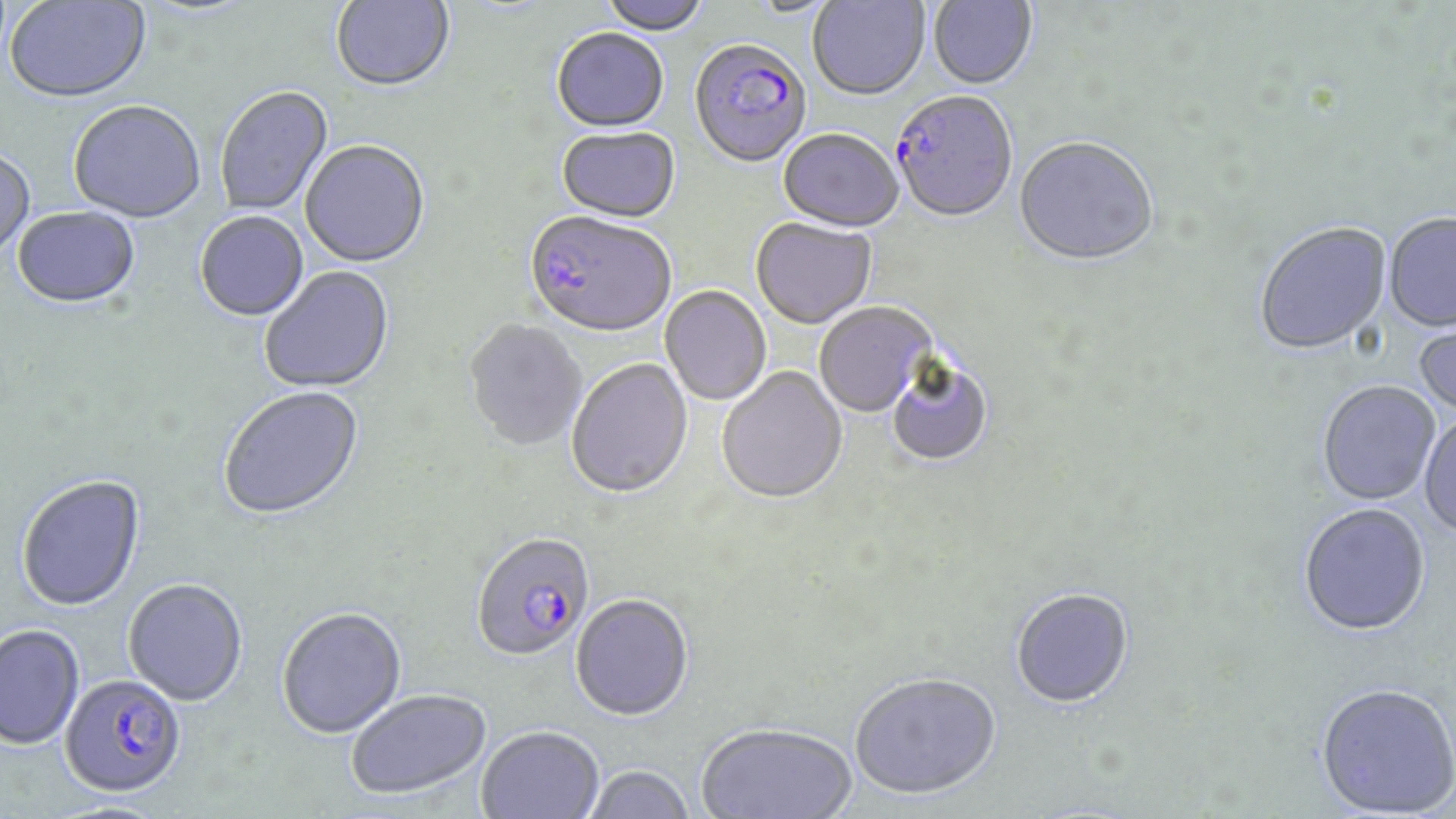
Approximate bounding boxes as (x1, y1, x2, y2) in pixels. Plasmodium falciparum-infected red blood cell locations: (689, 42, 811, 170), (890, 94, 1017, 225), (523, 213, 675, 341), (471, 536, 595, 663), (59, 677, 186, 800). Uninfected red blood cell locations: (331, 0, 455, 94), (599, 0, 710, 36), (808, 0, 929, 103), (927, 0, 1038, 91), (4, 1, 152, 106), (743, 1, 844, 19), (551, 30, 669, 134), (216, 87, 334, 216), (69, 103, 206, 225), (557, 128, 681, 225), (777, 131, 905, 235), (1014, 139, 1159, 269), (300, 142, 431, 270), (0, 150, 35, 264), (12, 208, 142, 311), (195, 213, 309, 323), (1383, 215, 1456, 334), (750, 218, 876, 331), (1254, 223, 1392, 357), (260, 267, 395, 394), (660, 286, 772, 406), (814, 303, 936, 419), (1413, 312, 1456, 418), (464, 320, 587, 453), (566, 360, 693, 501), (888, 361, 993, 468), (716, 368, 848, 506), (1317, 382, 1440, 507), (219, 387, 366, 523), (1418, 415, 1456, 540), (17, 476, 146, 613), (1298, 505, 1430, 639), (123, 581, 248, 708), (1011, 590, 1134, 711), (570, 596, 693, 724), (277, 609, 407, 741), (0, 626, 85, 751), (849, 676, 1001, 803), (1315, 686, 1456, 818), (346, 691, 492, 802), (696, 725, 858, 818), (477, 728, 603, 819), (582, 767, 695, 819). Slide-level diagnosis: Plasmodium falciparum. Captured at 1000x magnification. Optical microscopy. One field of a larger specimen. Thin blood smear. May-Grünwald-Giemsa-stained preparation. Image is 1456×819 pixels.